Assess the morphology of the erythrocytes.
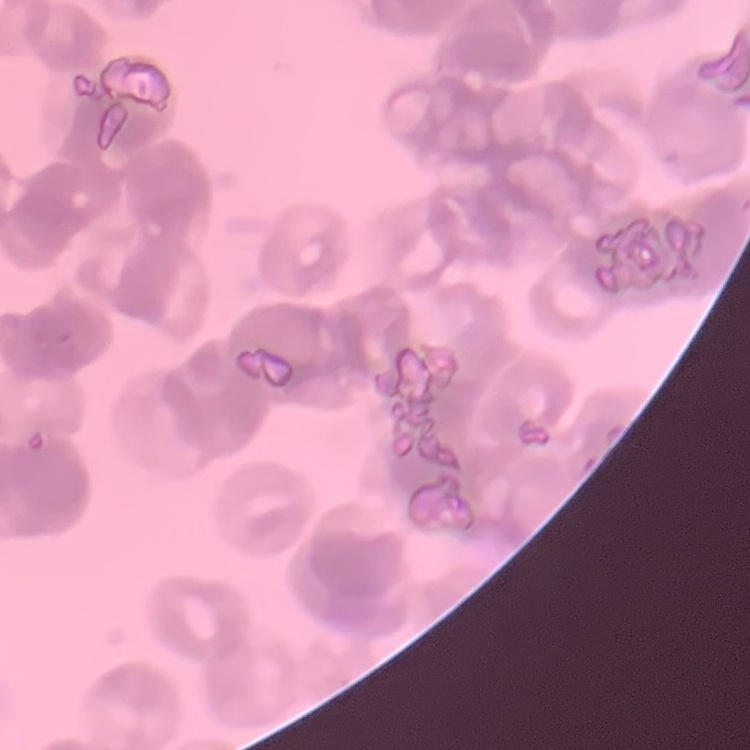
Rouleaux formation.

Summary:
  - Preparation: thin peripheral smear
  - Stain: Field's or Giemsa
  - Image type: one tile cut from a larger photomicrograph